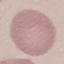 Malaria status: uninfected. Photographed with a smartphone camera at the microscope eyepiece. Automatically extracted cell patch, resized to 64 × 64 pixels. Giemsa-stained preparation. Thin blood smear.